Point out each malaria parasite.
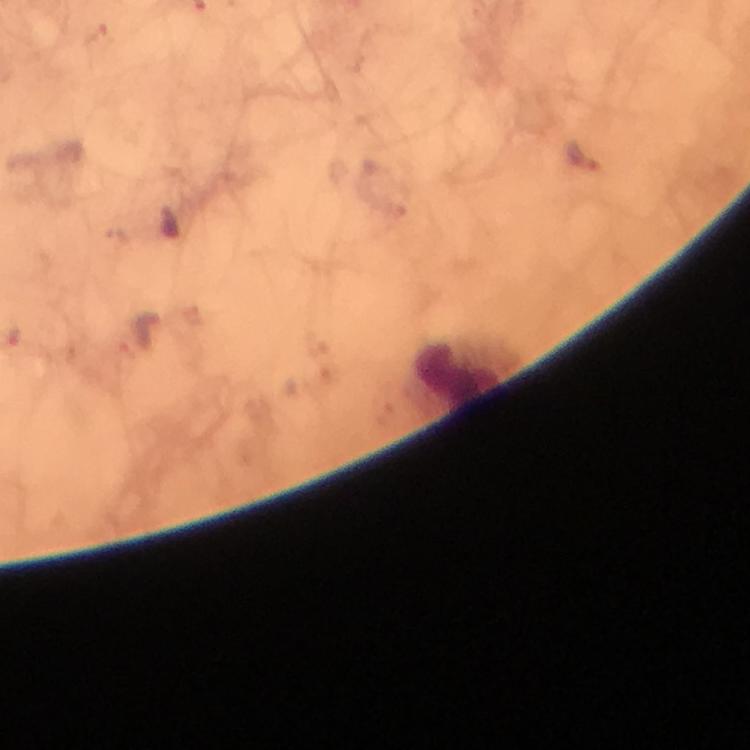

Approximate centers as [x, y] in pixels.
Malaria parasites: [579, 157].

stain = Giemsa
cropped from = one field of view
capture = smartphone camera through the microscope
immersion oil = applied
leukocyte locations = approximate centers as [x, y] in pixels: [458, 375]
image size = 750×750 pixels
context = from a diagnostic examination for malaria
preparation = thick blood film
magnification = 100x